Identify the parasite.
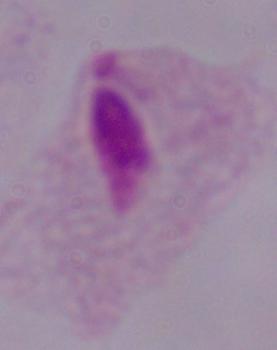
This is a trichomonad.

Captured at 1000x magnification. Photomicrograph.